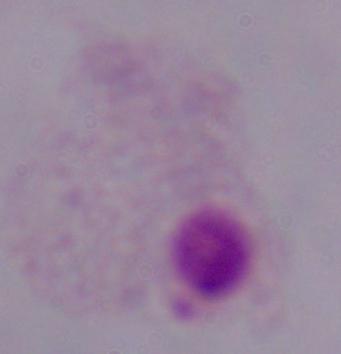
identification = trichomonad
magnification = 1000x
modality = micrograph